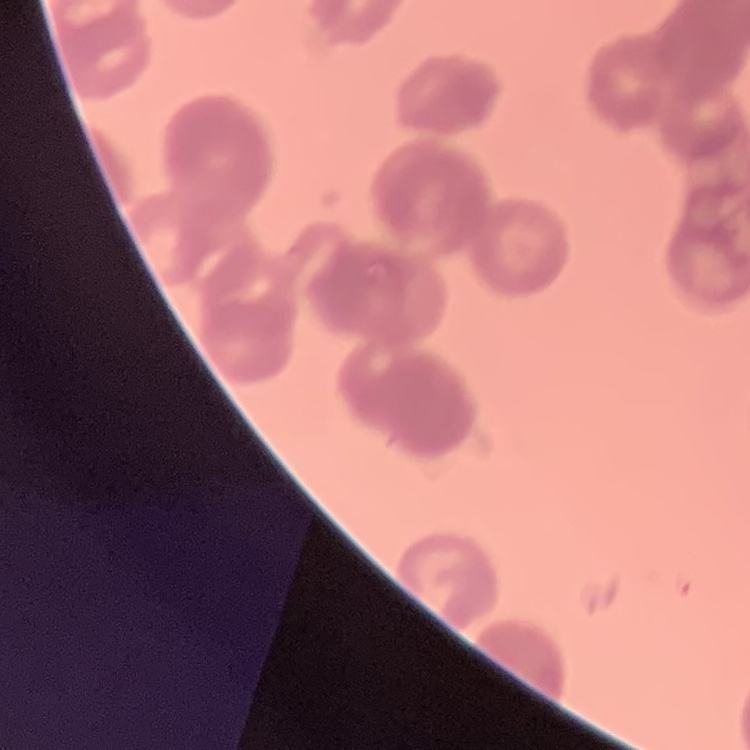
Summary:
  - Red blood cell morphology: rouleaux formation
  - Preparation: thin blood smear
  - Stain: Field's or Giemsa
  - Image type: square crop of a larger photomicrograph